Classify this cell by malaria status.
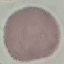
Uninfected.

Summary:
  - Preparation: thin blood smear
  - Stain: Giemsa
  - Capture: smartphone camera at the microscope eyepiece
  - Image type: automatically extracted cell patch, resized to 64 × 64 pixels